Name the parasite shown.
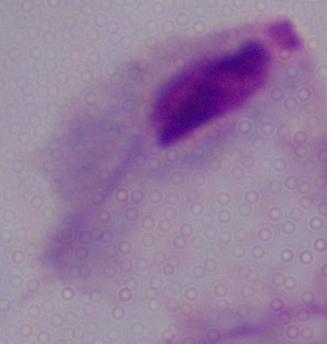
This is a trichomonad.

magnification = 1000x
modality = photomicrograph